Assess this cell for malaria.
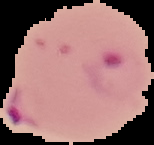

Parasitized.

Summary:
  - Image type: cell region segmented out of the field of view; surrounding area masked to black
  - Preparation: thin blood film
  - Image size: 154×145 pixels